Locate every malaria parasite.
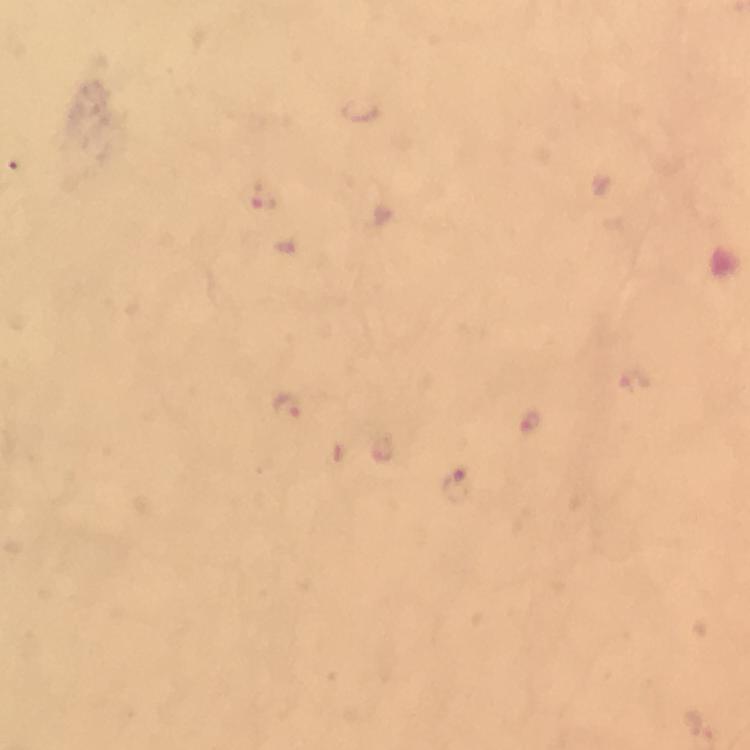

Approximate centers as (x, y) in pixels.
Malaria parasites: (262, 198), (630, 378), (288, 408), (529, 421), (383, 448), (454, 487).

From a malaria diagnostic workup. Giemsa-stained preparation. Cropped region of a single field of view. Immersion oil was used. Image is 750×750 pixels. At 100x magnification. Photographed with a smartphone mounted on the microscope. Thick blood film.